Assess the background quality.
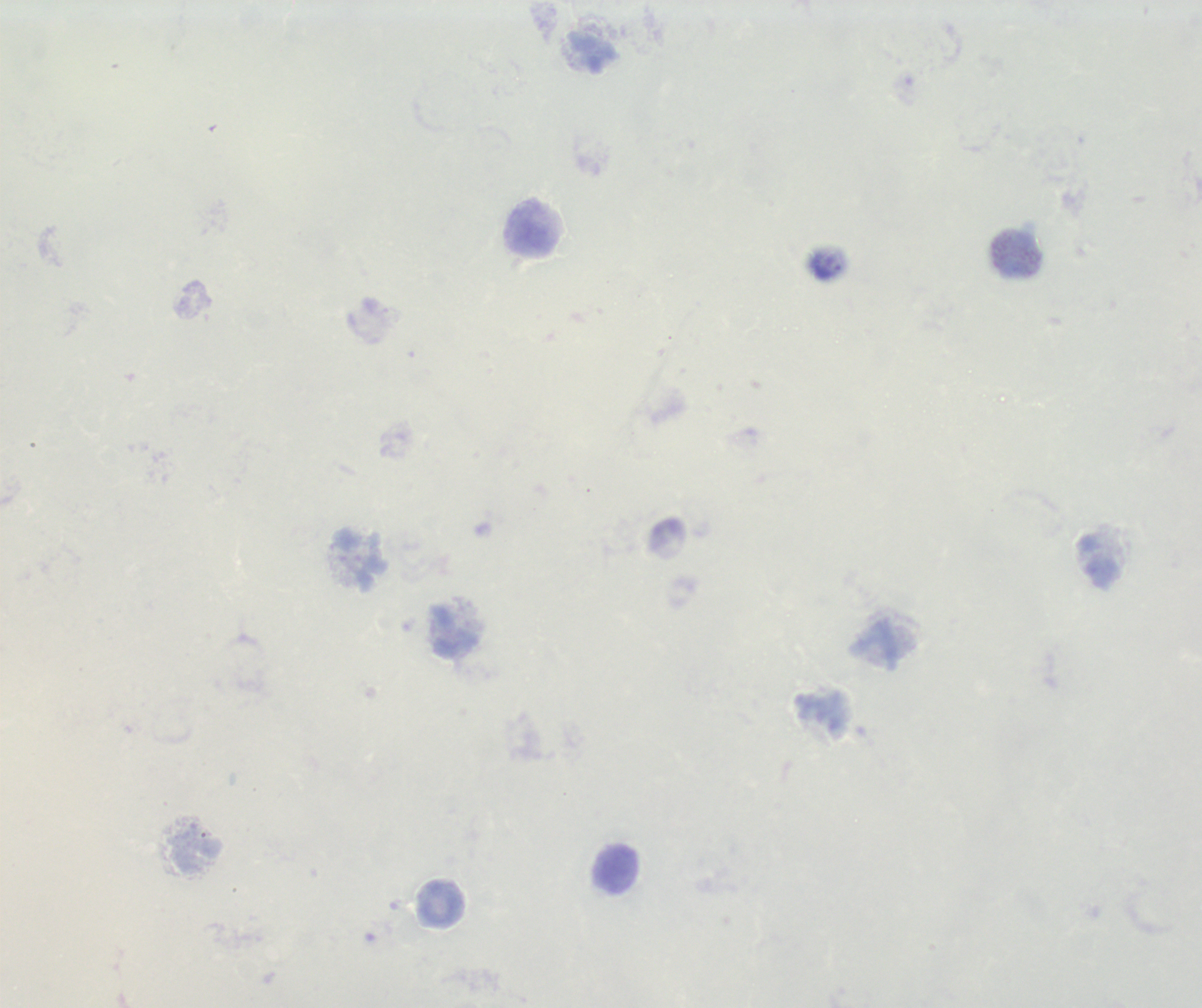

Unsatisfactory.

Approximate centers as (x, y) in pixels.
Summary:
  - Leukocyte locations: (592, 52), (531, 229), (1020, 253), (359, 557), (1099, 561), (454, 633), (199, 853), (616, 869)
  - Result: negative for Plasmodium parasites
  - Image size: 1202×1008 pixels
  - Context: previously used in a real diagnosis
  - Field of view: one from this slide
  - Magnification: 100x
  - Stain: Romanowsky
  - Preparation: thick smear of blood